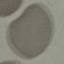
Result: no malaria parasites detected. Giemsa-stained preparation. Photographed with a smartphone camera at the microscope eyepiece. Thin blood smear. Cell patch, automatically extracted from a larger field of view and resized to 64 × 64 pixels.